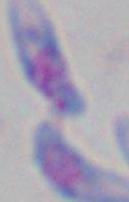
modality = micrograph
magnification = 1000x
identification = Toxoplasma gondii